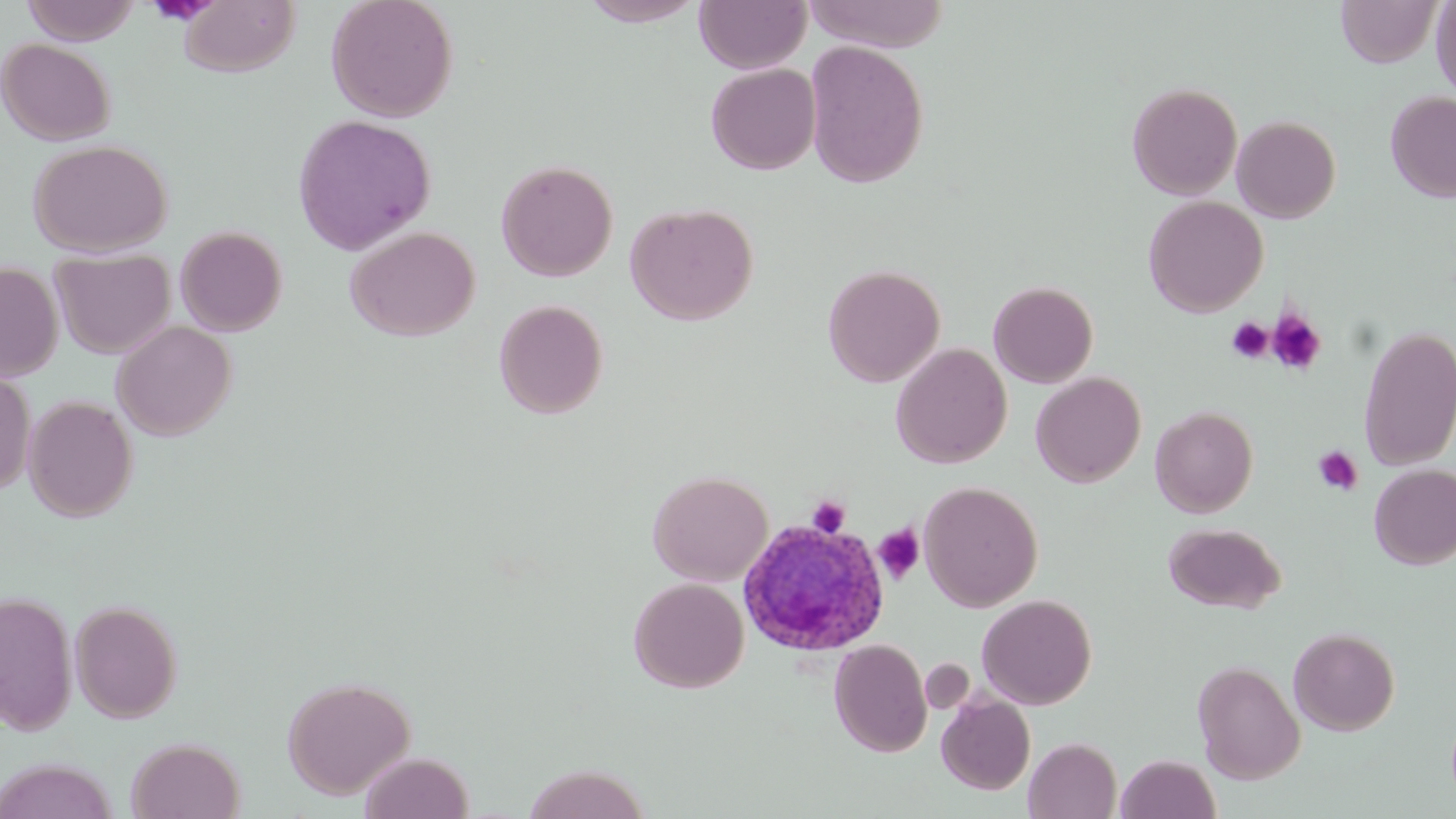

Approximate bounding boxes as (x1, y1, x2, y2) in pixels. Platelet locations: (145, 1, 220, 25), (1267, 310, 1327, 375), (1227, 317, 1273, 363), (1313, 446, 1363, 496), (806, 495, 851, 538), (874, 524, 925, 584). Uninfected red blood cell locations: (22, 0, 142, 45), (178, 0, 300, 77), (326, 0, 458, 122), (579, 0, 706, 26), (694, 0, 810, 73), (802, 0, 951, 51), (1336, 1, 1442, 67), (1431, 2, 1456, 101), (0, 38, 115, 146), (804, 41, 929, 188), (705, 62, 821, 175), (1126, 81, 1243, 201), (1385, 90, 1456, 202), (292, 114, 436, 255), (1231, 115, 1341, 223), (28, 138, 173, 256), (496, 159, 618, 281), (1143, 196, 1268, 317), (626, 202, 758, 326), (175, 225, 288, 336), (345, 225, 480, 341), (51, 248, 175, 359), (0, 263, 63, 382), (823, 263, 946, 388), (988, 280, 1099, 388), (494, 299, 608, 419), (112, 321, 236, 441), (1357, 325, 1456, 470), (891, 342, 1011, 469), (0, 368, 35, 496), (1030, 371, 1146, 487), (24, 395, 137, 521), (1150, 406, 1257, 518), (1369, 463, 1456, 570), (648, 470, 773, 586), (919, 480, 1043, 612), (1163, 522, 1286, 613), (628, 576, 749, 693), (0, 590, 78, 735), (976, 594, 1097, 709), (69, 599, 183, 723), (1288, 626, 1400, 735), (829, 639, 932, 757), (921, 659, 975, 714), (1192, 660, 1306, 783), (282, 675, 416, 799), (937, 693, 1035, 795), (126, 736, 245, 819), (1024, 737, 1122, 818), (360, 752, 474, 819), (1116, 753, 1220, 819), (1, 759, 119, 818), (522, 763, 652, 819). Plasmodium ovale-infected red blood cell locations: (736, 517, 892, 656). Slide-level diagnosis: Plasmodium ovale. 1000x magnification. Light microscopy. Thin blood smear. Single field of view. May-Grünwald-Giemsa stain. Image is 1456×819 pixels.